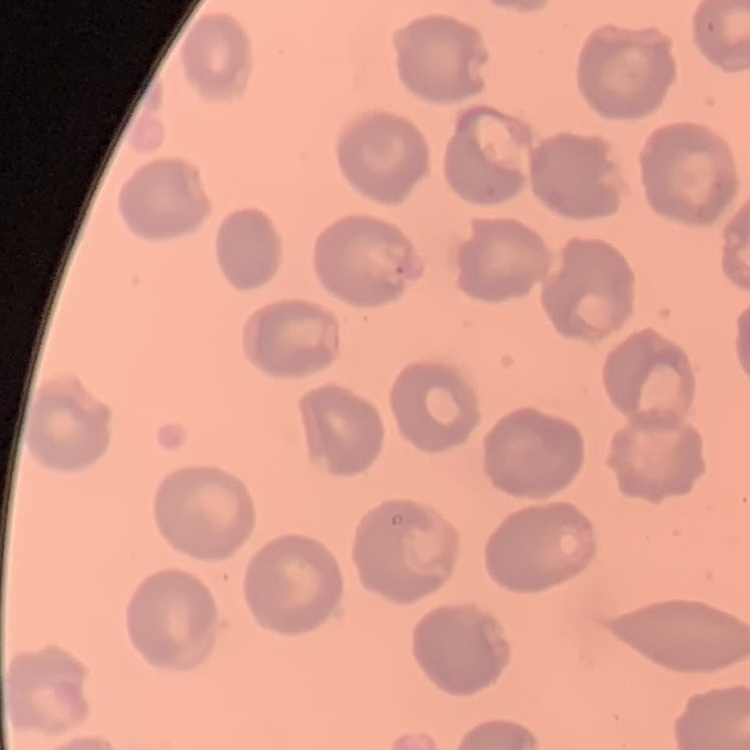
Summary:
  - Red blood cell morphology: no rouleaux formation
  - Image type: square crop of a larger photomicrograph
  - Stain: Field's or Giemsa
  - Preparation: thin blood smear